Draw a bounding box around every Plasmodium parasite.
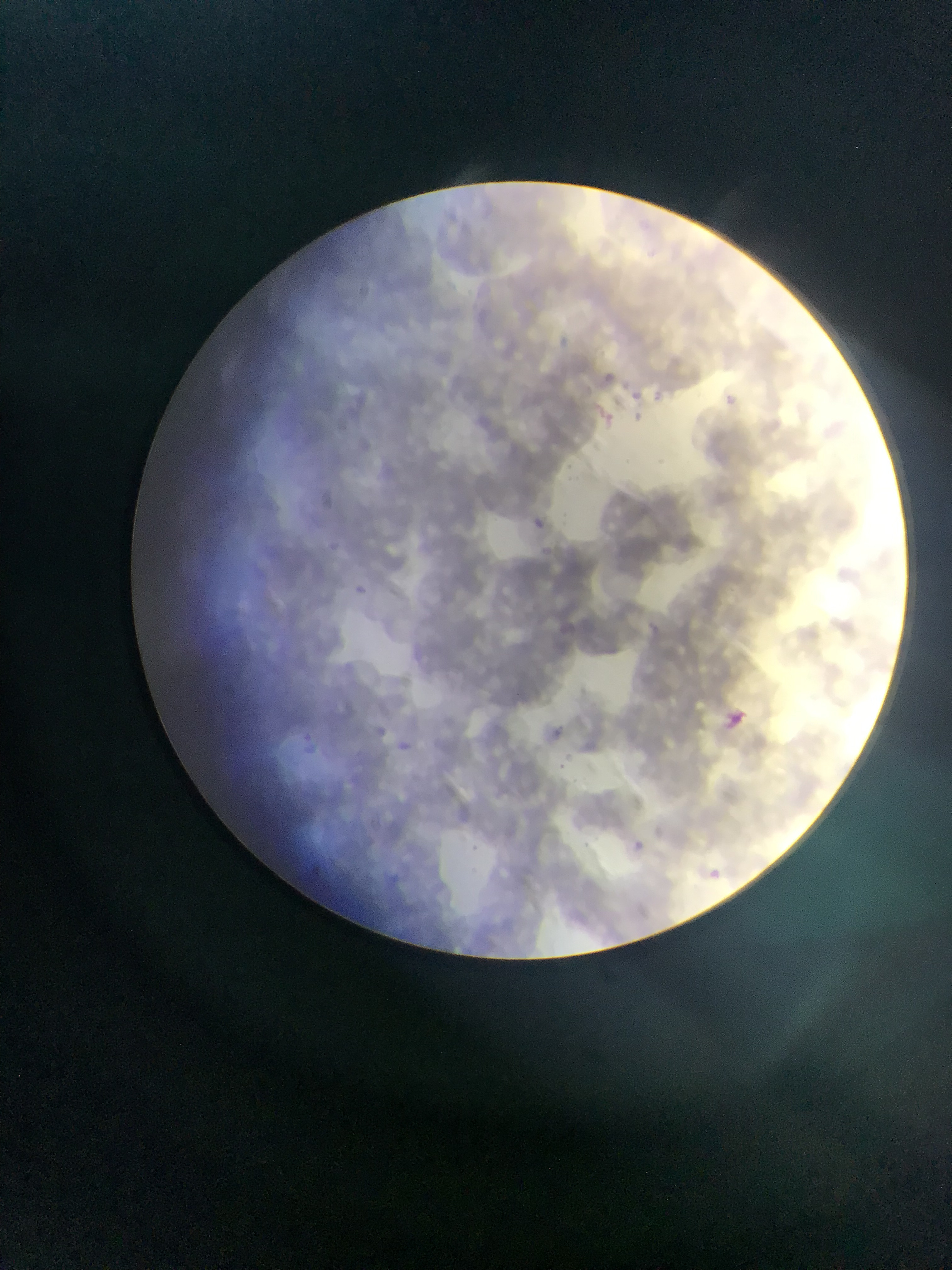
Approximate bounding boxes as [left, top, right, bottom] in pixels.
Plasmodium parasites: [600, 369, 617, 383], [630, 389, 646, 402], [724, 390, 738, 403], [598, 399, 610, 416], [634, 410, 658, 428], [529, 515, 548, 532], [330, 541, 342, 556], [357, 580, 369, 594], [715, 702, 753, 740], [553, 720, 573, 738], [398, 739, 419, 753], [633, 834, 645, 851], [696, 860, 730, 890].

country: Ghana
capture: mobile-phone photograph through a microscope
field_of_view: single
image_size: 952×1270 pixels
preparation: thin blood smear